Outline each blood parasite and name the species.
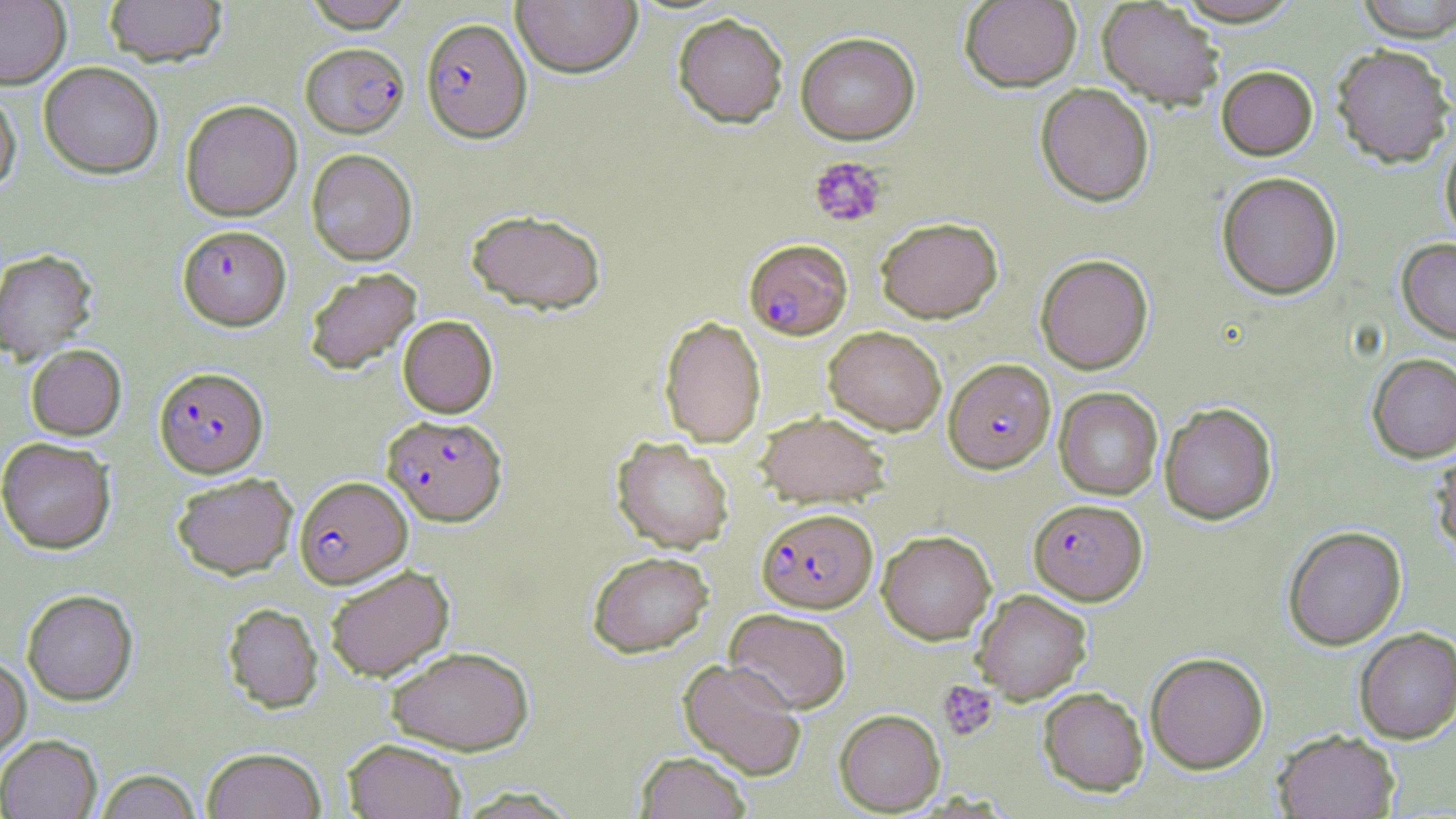

Approximate bounding boxes as [x1, y1, x2, y2] in pixels.
Plasmodium falciparum-infected red blood cells: [421, 17, 532, 142], [301, 42, 409, 137], [177, 225, 291, 330], [744, 239, 852, 339], [943, 358, 1056, 473], [154, 366, 268, 477], [382, 414, 507, 526], [294, 475, 411, 588], [1028, 498, 1147, 605], [756, 508, 878, 612].
No Plasmodium ovale, Plasmodium malariae, Plasmodium vivax, Babesia divergens, or Trypanosoma brucei observed.

Summary:
  - Uninfected red blood cell locations: [0, 0, 70, 88], [104, 0, 227, 67], [303, 0, 413, 32], [511, 0, 642, 78], [959, 0, 1082, 92], [1355, 0, 1456, 41], [1097, 1, 1224, 109], [672, 13, 788, 128], [795, 31, 920, 144], [1332, 44, 1454, 167], [39, 62, 163, 178], [1217, 66, 1317, 160], [1036, 83, 1154, 206], [0, 87, 21, 194], [180, 99, 302, 221], [1440, 135, 1456, 245], [306, 148, 417, 266], [1217, 171, 1342, 299], [466, 208, 607, 315], [875, 216, 1003, 323], [1397, 238, 1456, 342], [0, 249, 98, 363], [1035, 253, 1154, 374], [304, 267, 422, 375], [398, 315, 498, 418], [659, 315, 766, 448], [824, 326, 947, 435], [26, 344, 127, 440], [1367, 353, 1456, 462], [1054, 387, 1163, 500], [1159, 402, 1277, 524], [755, 410, 891, 508], [612, 435, 734, 553], [0, 437, 116, 554], [1429, 447, 1456, 562], [171, 472, 299, 579], [1282, 525, 1407, 650], [877, 530, 997, 644], [586, 551, 714, 658], [324, 564, 455, 682], [972, 589, 1092, 704], [22, 590, 138, 705], [222, 602, 323, 713], [725, 607, 852, 714], [1354, 627, 1455, 744], [386, 645, 534, 755], [1145, 651, 1269, 774], [0, 654, 31, 763], [679, 658, 807, 780], [1038, 687, 1149, 796], [834, 709, 945, 815], [1273, 729, 1400, 818], [0, 734, 102, 819], [342, 738, 467, 819], [202, 746, 327, 819], [636, 751, 751, 819], [94, 769, 202, 819], [454, 786, 580, 818]
  - Platelet locations: [808, 156, 888, 228], [938, 680, 998, 742]
  - Slide-level diagnosis: Plasmodium falciparum
  - Image size: 1456×819 pixels
  - Magnification: 1000x
  - Field of view: single
  - Preparation: thin blood film
  - Stain: May-Grünwald-Giemsa
  - Modality: optical microscopy